Point out each leukocyte.
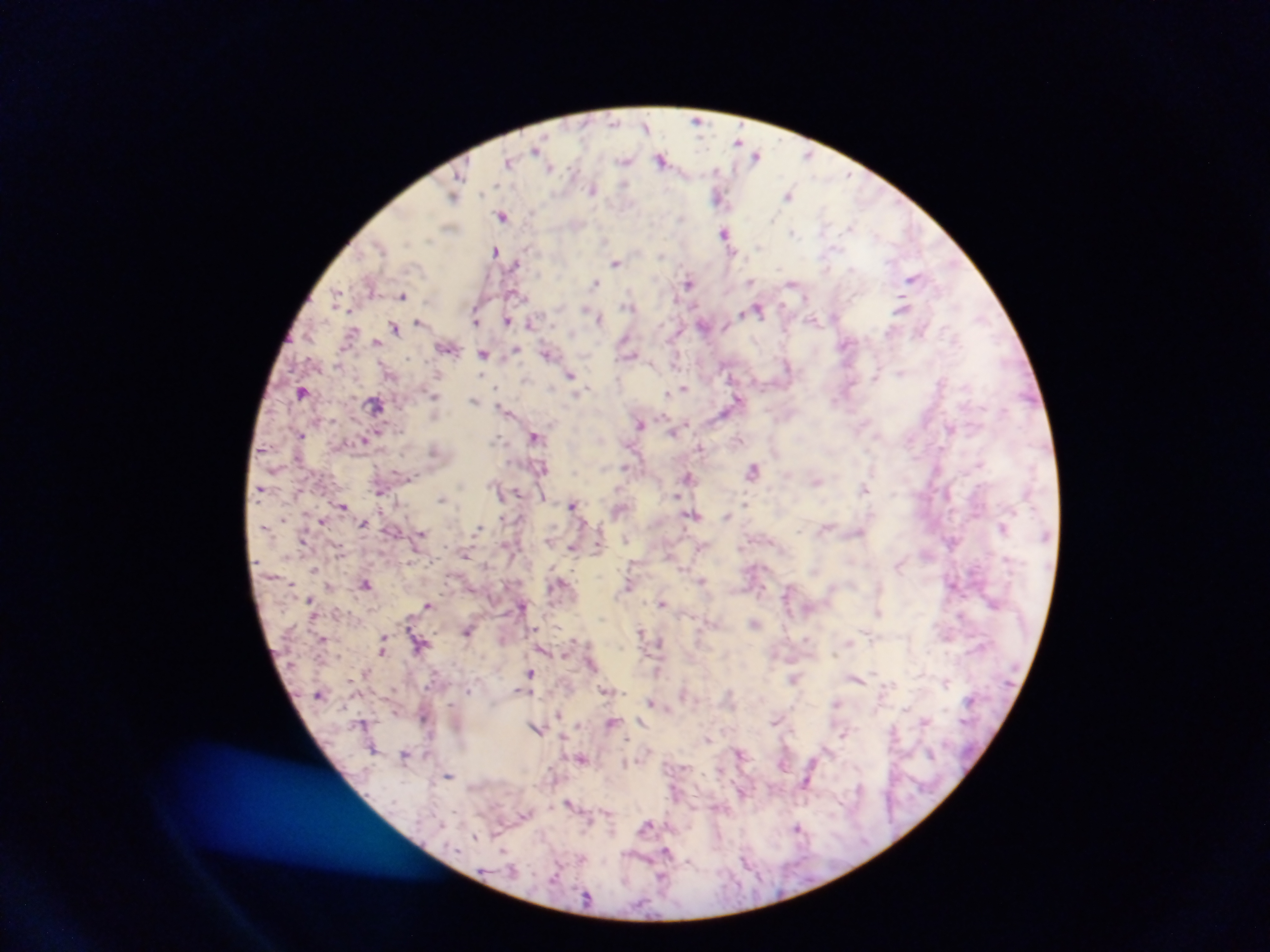
No leukocytes observed.

malaria parasite locations = approximate centers as [x, y] in pixels: [698, 120], [646, 125], [741, 141], [537, 150], [758, 154], [809, 155], [661, 158], [625, 160], [509, 161], [550, 168], [593, 189], [789, 194], [454, 195], [719, 196], [503, 216], [727, 234], [496, 250], [616, 262], [518, 263], [913, 278], [751, 281], [688, 282], [792, 282], [596, 283], [403, 294], [339, 297], [630, 305], [903, 306], [758, 308], [599, 316], [476, 319], [508, 320], [815, 320], [420, 322], [531, 323], [705, 325], [395, 328], [353, 330], [377, 343], [847, 345], [449, 346], [516, 350], [484, 353], [548, 353], [630, 354], [571, 374], [438, 375], [877, 375], [684, 387], [302, 391], [669, 392], [435, 396], [475, 400], [738, 401], [377, 405], [506, 411], [640, 424], [951, 427], [674, 430], [301, 434], [536, 436], [365, 439], [701, 447], [434, 450], [625, 467], [543, 468], [754, 470], [688, 476], [817, 480], [865, 488], [380, 492], [678, 495], [442, 499], [342, 504], [573, 504], [619, 509], [695, 514], [727, 516], [282, 519], [322, 520], [363, 523], [1004, 526], [478, 528], [421, 534], [304, 539], [572, 546], [465, 554], [927, 554], [900, 566], [314, 568], [703, 581], [560, 582], [366, 583], [953, 584], [629, 585], [788, 594], [311, 600], [662, 603], [429, 604], [522, 606], [878, 611], [756, 622], [641, 630], [467, 631], [323, 638], [385, 640], [660, 642], [384, 648], [544, 650], [566, 653], [592, 664], [657, 670], [531, 672], [795, 678], [857, 678], [946, 681], [606, 690], [521, 691], [652, 702], [836, 702], [395, 710], [559, 714], [926, 720], [777, 721], [612, 722], [363, 724], [537, 728], [843, 733], [708, 738], [374, 748], [405, 754], [583, 758], [450, 774], [807, 781], [571, 804], [647, 826], [799, 828], [668, 854]
country = Ghana
capture = mobile-phone photograph through a microscope
image size = 1270×952 pixels
preparation = thick blood smear
field of view = single